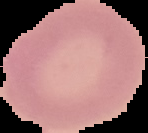
preparation = thin blood film
image size = 148×133 pixels
result = no malaria parasites detected
image type = cell region segmented out of the field of view; surrounding area masked to black